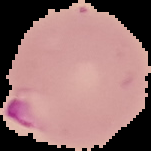

result = malaria parasites identified
image size = 151×151 pixels
image type = cell region segmented out of the field of view; surrounding area masked to black
preparation = thin blood film